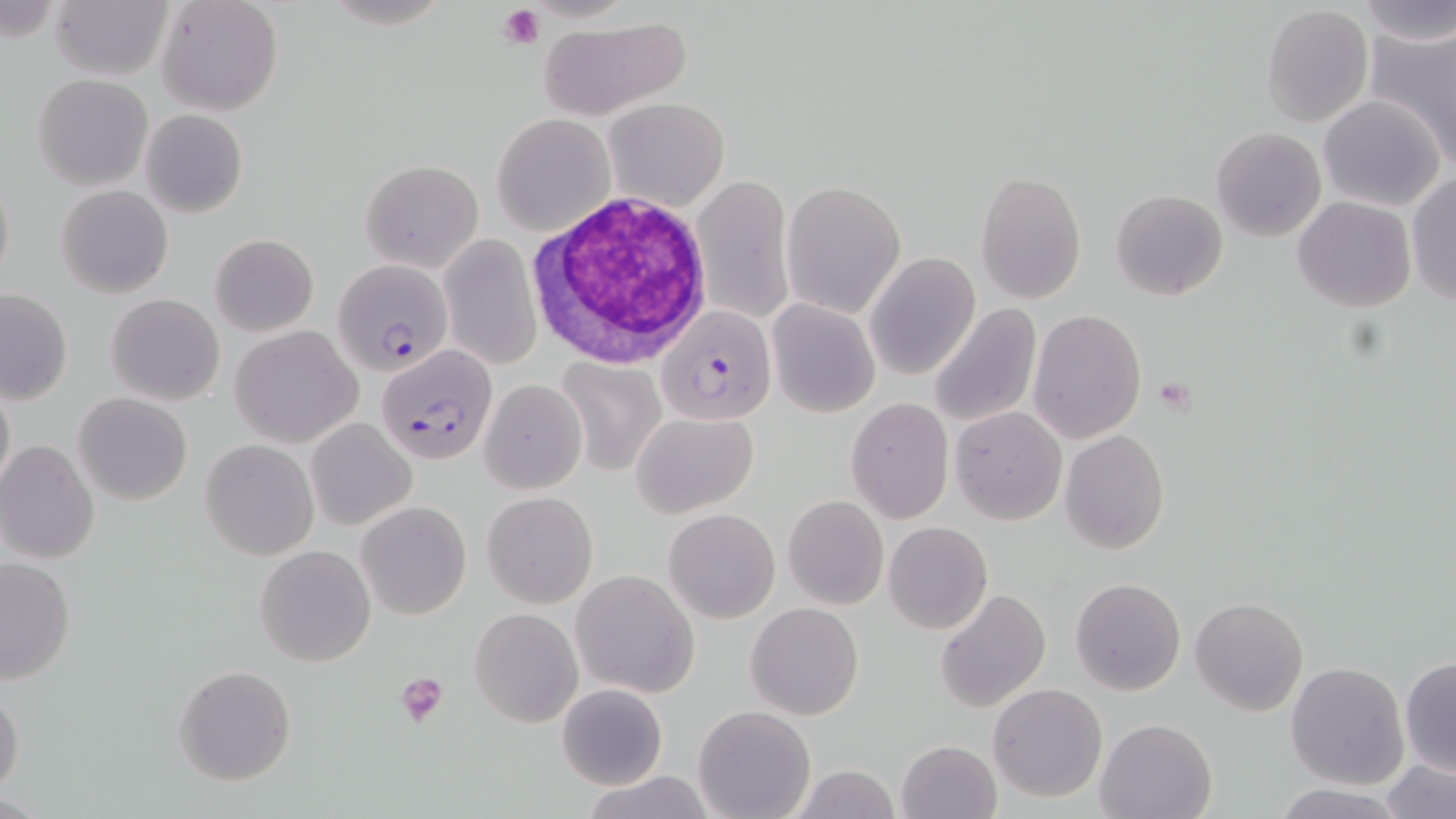
slide_level_diagnosis: Plasmodium falciparum
stain: May-Grünwald-Giemsa
magnification: 1000x
uninfected_red_blood_cell_locations: 'approximate bounding boxes as [x1, y1, x2, y2] in pixels: [50, 0, 174, 81], [155, 0, 283, 117], [1352, 0, 1454, 43], [1261, 6, 1373, 127], [539, 16, 691, 120], [1362, 23, 1456, 164], [32, 73, 154, 191], [1315, 95, 1442, 211], [604, 96, 729, 211], [140, 108, 248, 218], [492, 112, 615, 236], [1211, 127, 1326, 242], [358, 158, 483, 273], [1, 166, 15, 294], [691, 172, 795, 327], [976, 172, 1086, 302], [1408, 173, 1455, 308], [782, 179, 906, 318], [56, 184, 173, 300], [1111, 189, 1228, 301], [1292, 196, 1417, 312], [209, 233, 319, 336], [439, 236, 540, 369], [864, 252, 979, 380], [0, 289, 73, 405], [105, 293, 224, 406], [767, 299, 880, 419], [928, 303, 1042, 428], [1028, 310, 1147, 443], [231, 324, 363, 447], [555, 360, 667, 476], [0, 376, 15, 500], [479, 379, 586, 494], [73, 392, 192, 506], [845, 399, 954, 523], [949, 406, 1066, 525], [631, 410, 760, 518], [306, 417, 417, 531], [1061, 429, 1170, 554], [200, 438, 318, 561], [0, 439, 98, 567], [481, 490, 597, 607], [782, 495, 889, 610], [357, 501, 471, 620], [664, 508, 780, 623], [884, 521, 993, 634], [254, 545, 375, 666], [0, 556, 76, 685], [572, 569, 699, 697], [1071, 577, 1186, 696], [934, 587, 1050, 714], [1191, 597, 1307, 716], [745, 601, 864, 720], [470, 607, 582, 727], [1399, 656, 1455, 776], [1285, 660, 1408, 790], [173, 664, 295, 786], [556, 683, 669, 791], [0, 684, 23, 799], [989, 684, 1107, 802], [693, 705, 816, 819], [1096, 717, 1218, 819], [896, 740, 1002, 819], [1379, 757, 1455, 819], [787, 764, 903, 819], [578, 769, 718, 818], [1270, 784, 1408, 818]'
white_blood_cell_locations: 'approximate bounding boxes as [x1, y1, x2, y2] in pixels: [526, 191, 720, 369]'
modality: optical microscopy
image_size: 1456×819 pixels
plasmodium_falciparum_infected_red_blood_cell_locations: 'approximate bounding boxes as [x1, y1, x2, y2] in pixels: [332, 256, 453, 375], [657, 306, 775, 426], [376, 342, 501, 467]'
field_of_view: one of a larger specimen
preparation: thin blood film
platelet_locations: 'approximate bounding boxes as [x1, y1, x2, y2] in pixels: [499, 3, 545, 48], [1152, 376, 1198, 414], [397, 671, 449, 728]'